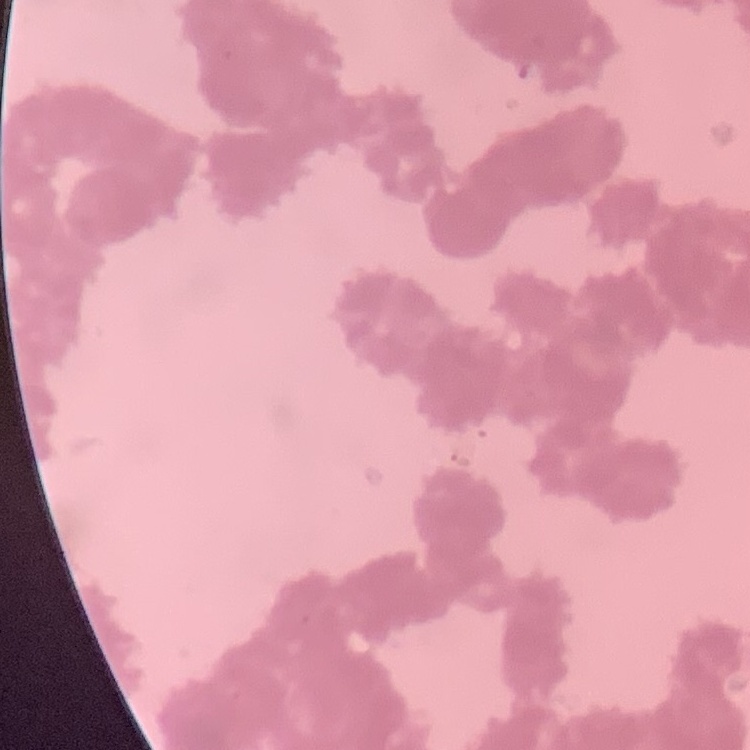

red blood cell morphology = rouleaux formation
preparation = thin peripheral smear
stain = Field's or Giemsa
image type = one tile cut from a larger photomicrograph